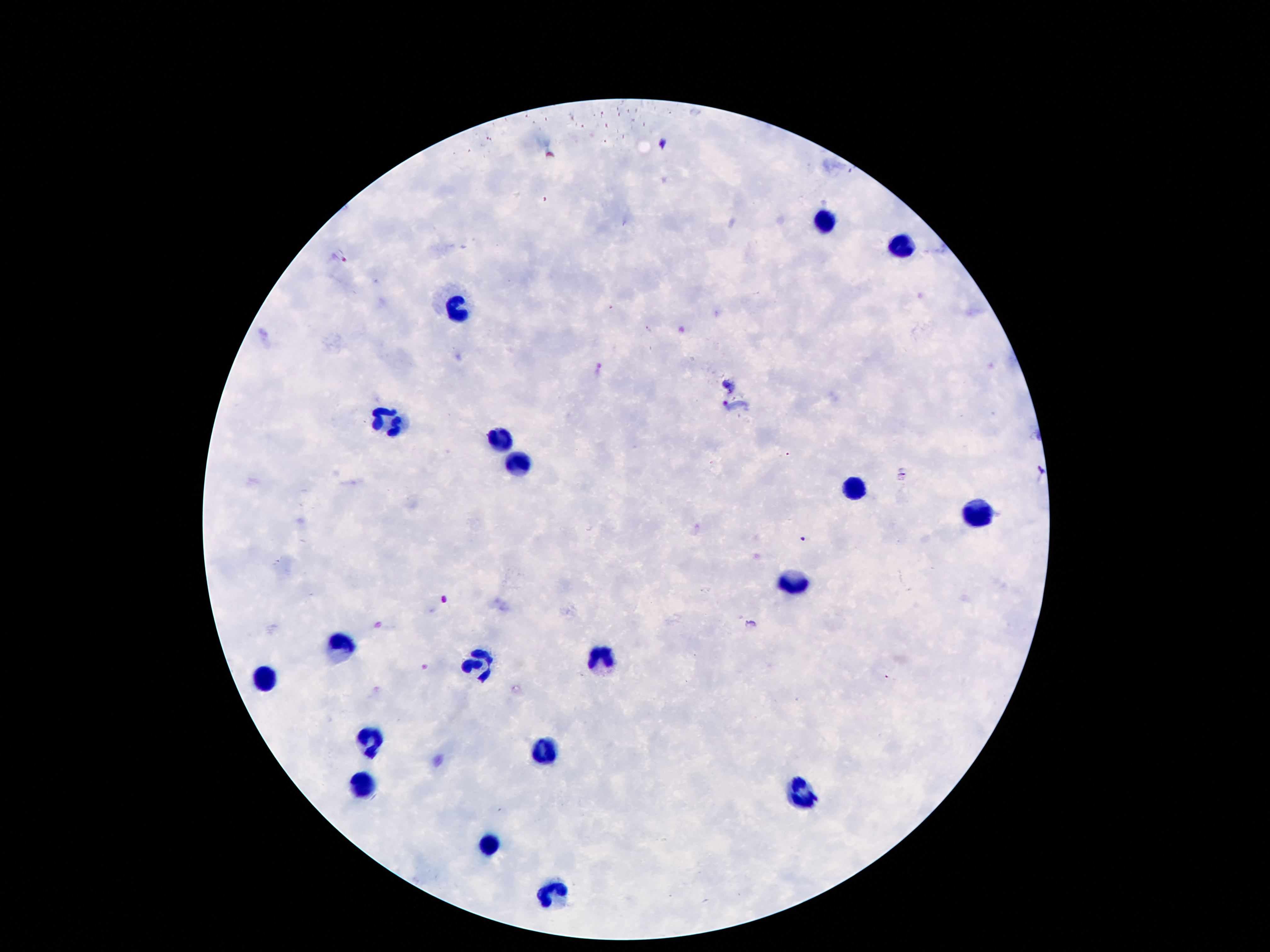
patient_malaria_status: uninfected
capture: smartphone camera through the microscope eyepiece
preparation: thick blood film
stain: Giemsa
magnification: 100x
image_size: 1270×952 pixels
field_of_view: one from this slide
leukocyte_locations: 'approximate centers as (x, y) in pixels: (819, 222), (896, 249), (460, 309), (388, 422), (499, 440), (519, 462), (851, 490), (971, 511), (794, 583), (342, 647), (601, 656), (476, 662), (263, 678), (372, 739), (540, 751), (363, 788), (801, 794), (487, 844), (556, 890)'